Name the parasite shown.
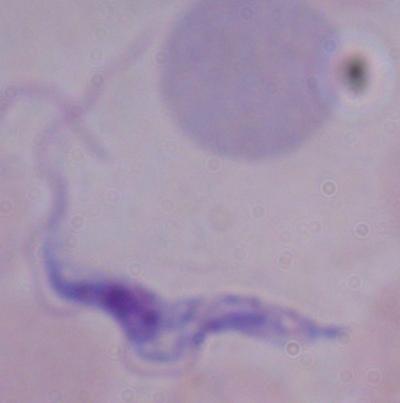

A trypanosome.

modality: photomicrograph
magnification: 1000x